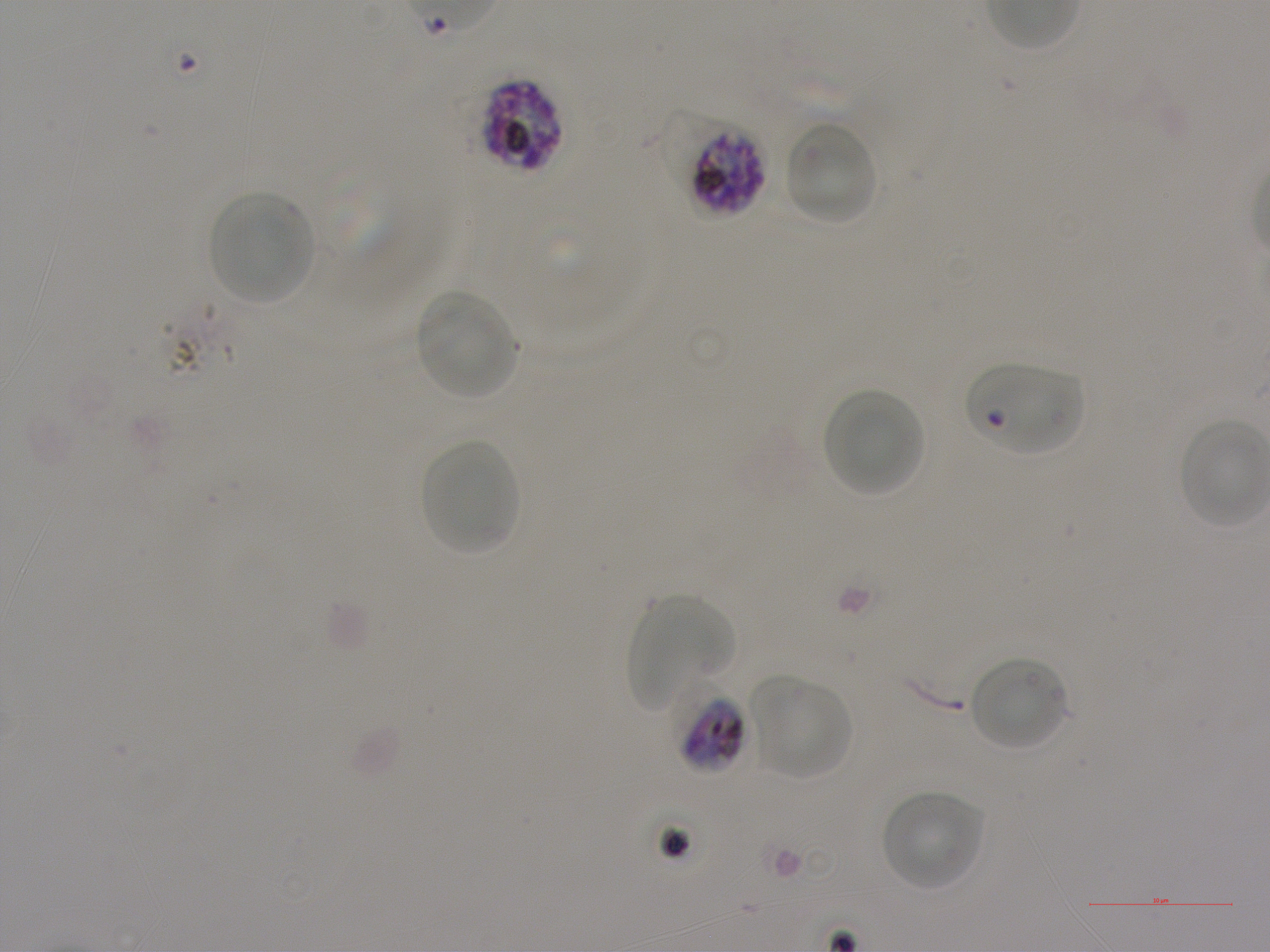

Not every red blood cell is marked. A life-cycle stage — or a range of stages, where the recorded stages span more than one — follows each staged infected red blood cell.
preparation = thin blood film
locations of red blood cells of indeterminate infection status = approximate bounding boxes as {x1, y1, x2, y2} in pixels: {964, 363, 1082, 456}
stain = Giemsa
image size = 1270×952 pixels
culture = Plasmodium falciparum strain NF54, static, in vitro
objective = 100x, oil immersion, numerical aperture 1.25
field of view = one from this slide
locations of uninfected red blood cells = approximate bounding boxes as {x1, y1, x2, y2} in pixels: {784, 119, 880, 225}, {207, 191, 313, 305}, {415, 290, 519, 399}, {823, 389, 924, 496}, {420, 438, 519, 555}, {627, 595, 732, 709}, {968, 656, 1069, 751}, {750, 675, 852, 780}, {881, 791, 984, 891}
donor blood group = A+
locations of infected red blood cells = approximate bounding boxes as {x1, y1, x2, y2} in pixels: {481, 79, 563, 172} late schizont; {661, 110, 767, 218} late trophozoite to late schizont; {674, 689, 748, 775} late trophozoite to early schizont